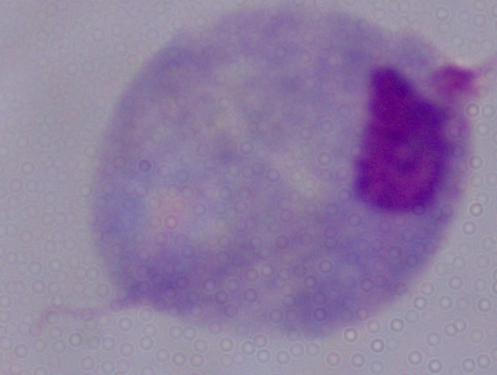

Summary:
  - Identification: trichomonad
  - Magnification: 1000x
  - Modality: photomicrograph